Report the malaria status of this cell.
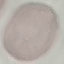

It is uninfected.

image type = cell patch, automatically extracted from a larger field of view and resized to 64 × 64 pixels
capture = smartphone through the microscope eyepiece
stain = Giemsa
preparation = thin blood smear